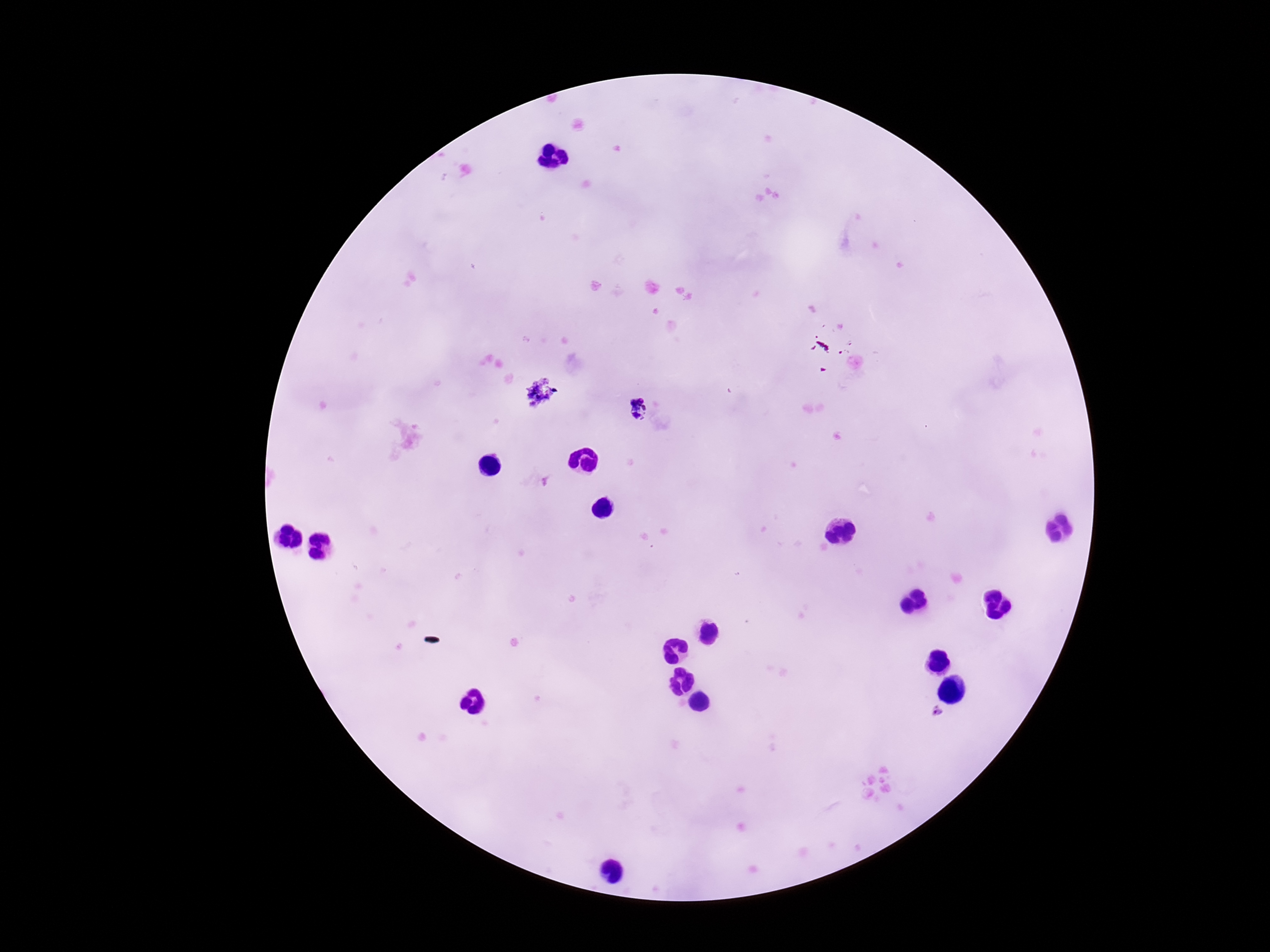
Approximate centers as [x, y] in pixels.
Summary:
  - Plasmodium parasite locations: [635, 407], [938, 711]
  - Magnification: 100x
  - Field of view: one from this slide
  - Preparation: thick peripheral-blood smear
  - Image size: 1270×952 pixels
  - Capture: smartphone camera through the microscope eyepiece
  - Patient malaria status: infected
  - Stain: Giemsa